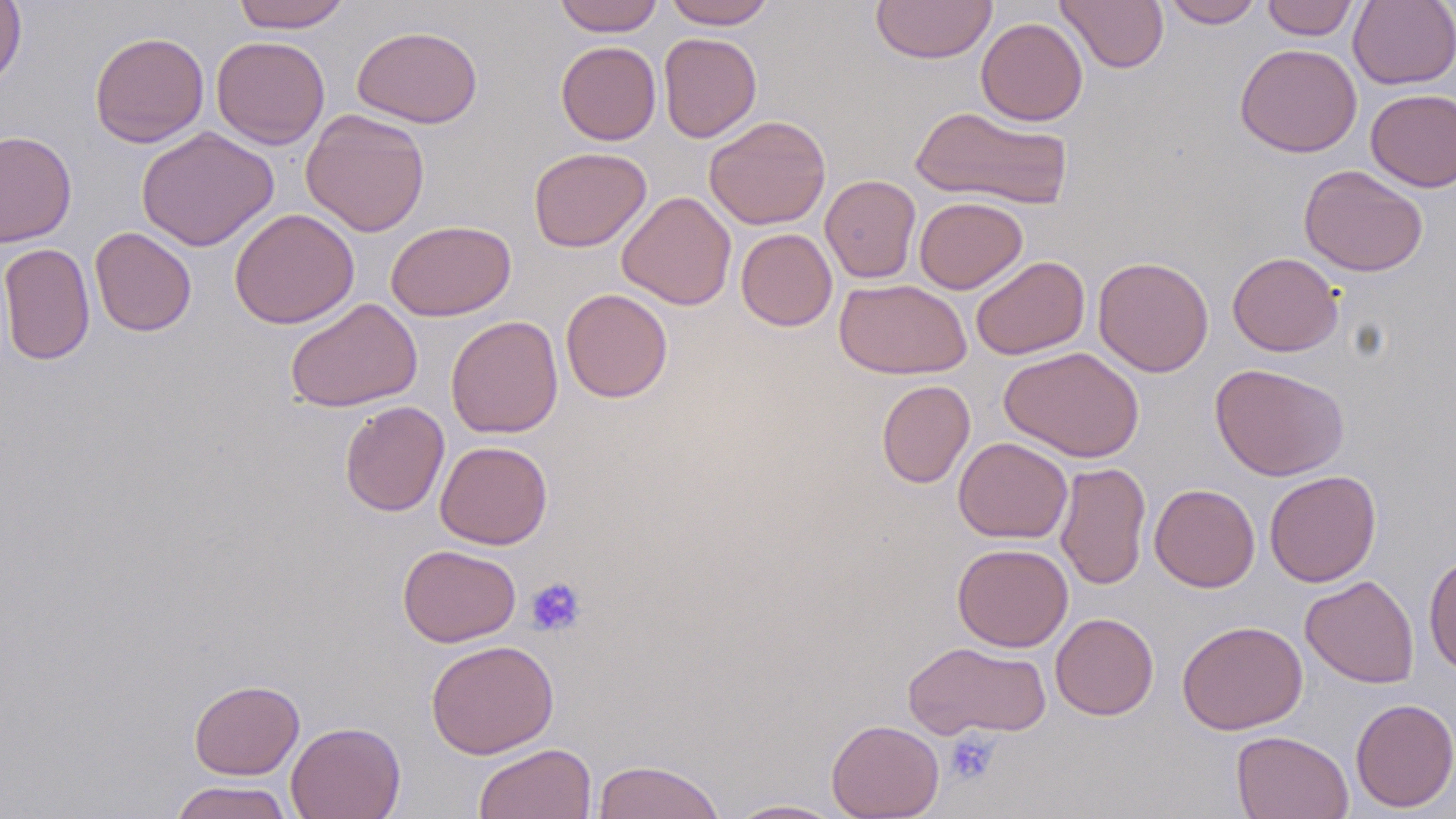
Approximate bounding boxes as (x1,y1)-(x2,y2) corner pairs in pixels. Uninfected red blood cell locations: (0,0)-(27,93), (232,0)-(351,32), (554,0)-(663,36), (663,0)-(777,29), (870,0)-(998,64), (1055,0)-(1169,73), (1162,0)-(1264,28), (1261,0)-(1359,40), (1348,0)-(1456,89), (976,17)-(1088,126), (352,25)-(483,128), (89,31)-(209,147), (658,32)-(762,142), (211,35)-(330,149), (556,41)-(661,145), (1234,43)-(1362,157), (1365,89)-(1456,192), (910,105)-(1073,210), (301,109)-(430,237), (704,115)-(831,230), (136,126)-(279,251), (0,131)-(76,247), (528,146)-(652,252), (1299,164)-(1428,277), (820,175)-(921,283), (617,191)-(737,310), (914,196)-(1027,294), (229,208)-(359,329), (386,220)-(516,321), (90,227)-(197,336), (735,228)-(838,331), (0,243)-(96,365), (1227,251)-(1343,356), (970,255)-(1090,360), (1093,256)-(1214,377), (834,278)-(972,379), (560,288)-(673,403), (285,298)-(423,412), (445,315)-(563,438), (999,347)-(1144,463), (1210,362)-(1349,481), (876,379)-(975,488), (340,400)-(449,517), (953,437)-(1073,543), (435,441)-(553,549), (1054,461)-(1151,591), (1264,469)-(1381,587), (1149,484)-(1260,592), (952,542)-(1074,652), (397,544)-(521,647), (1423,553)-(1456,674), (1300,575)-(1420,688), (1050,613)-(1159,720), (1177,619)-(1308,735), (425,639)-(559,759), (903,640)-(1051,740), (189,679)-(304,779), (1350,697)-(1456,812), (827,719)-(944,818), (286,721)-(406,819), (1231,729)-(1354,818), (473,742)-(596,819), (591,759)-(727,819), (169,780)-(295,819), (724,798)-(847,818). Platelet locations: (524,576)-(587,637), (943,729)-(1002,784). Slide-level diagnosis: no evidence of blood parasites. Optical microscopy. Image is 1456×819 pixels. 1000x magnification. May-Grünwald-Giemsa stain. Single field of view. Thin blood film.